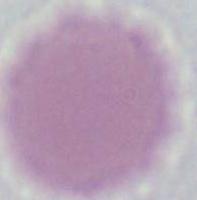
Summary:
  - Magnification: 1000x
  - Modality: photomicrograph
  - Identification: red blood cell